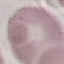
Summary:
  - Result: negative for malaria parasites
  - Capture: smartphone through the microscope eyepiece
  - Preparation: thin blood smear
  - Image type: cell patch, automatically extracted from a larger field of view and resized to 64 × 64 pixels
  - Stain: Giemsa